Report the malaria status of this cell.
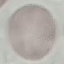

Uninfected.

Summary:
  - Preparation: thin blood smear
  - Image type: automatically extracted cell patch, resized to 64 × 64 pixels
  - Stain: Giemsa
  - Capture: smartphone camera at the microscope eyepiece